Comment on the morphology of the erythrocytes.
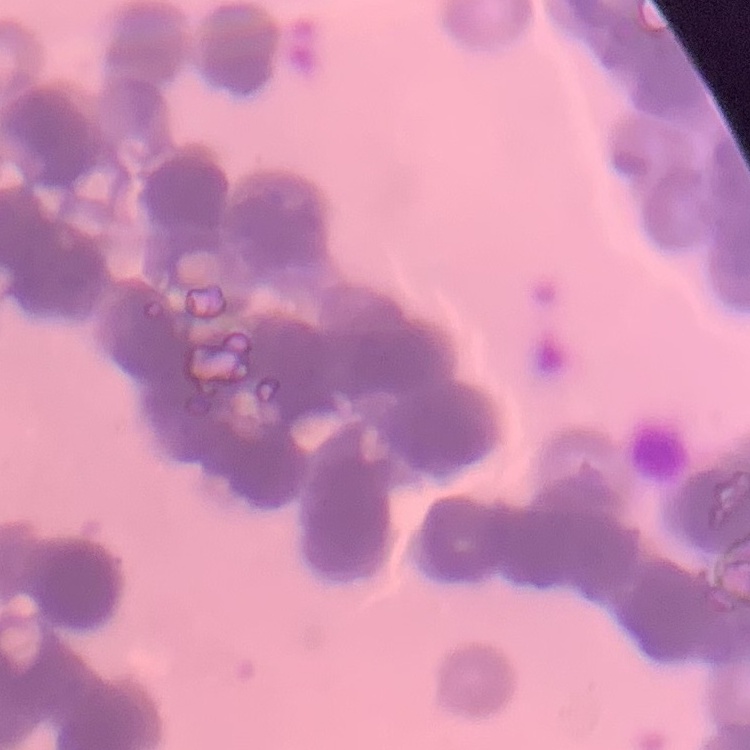

Rouleaux formation.

Summary:
  - Preparation: thin blood film
  - Stain: Field's or Giemsa
  - Image type: square crop of a larger photomicrograph